Point out each Plasmodium parasite.
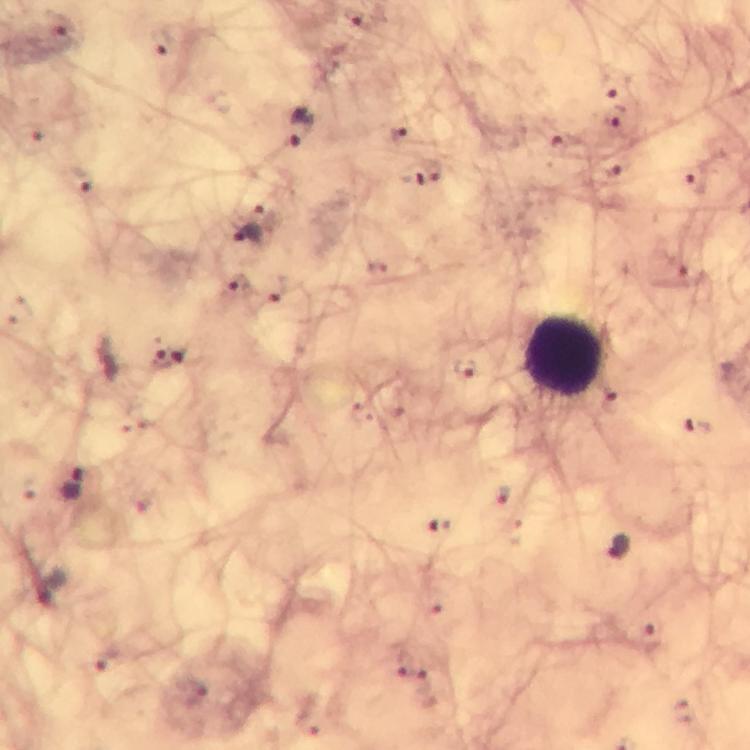
Approximate centers as (x, y) in pixels.
Plasmodium parasites: (355, 18), (164, 42), (617, 116), (300, 128), (399, 135), (564, 142), (433, 170), (414, 172), (696, 182), (247, 234), (171, 360), (464, 367), (695, 427), (618, 546).

Leukocyte locations: (563, 357). Photographed with a smartphone mounted on the microscope. At 100x magnification. Immersion oil applied. From a malaria diagnostic workup. Cropped region of a single field of view. Image is 750×750 pixels. Giemsa stain. Thick blood film.